Outline each Plasmodium ovale-infected red blood cell.
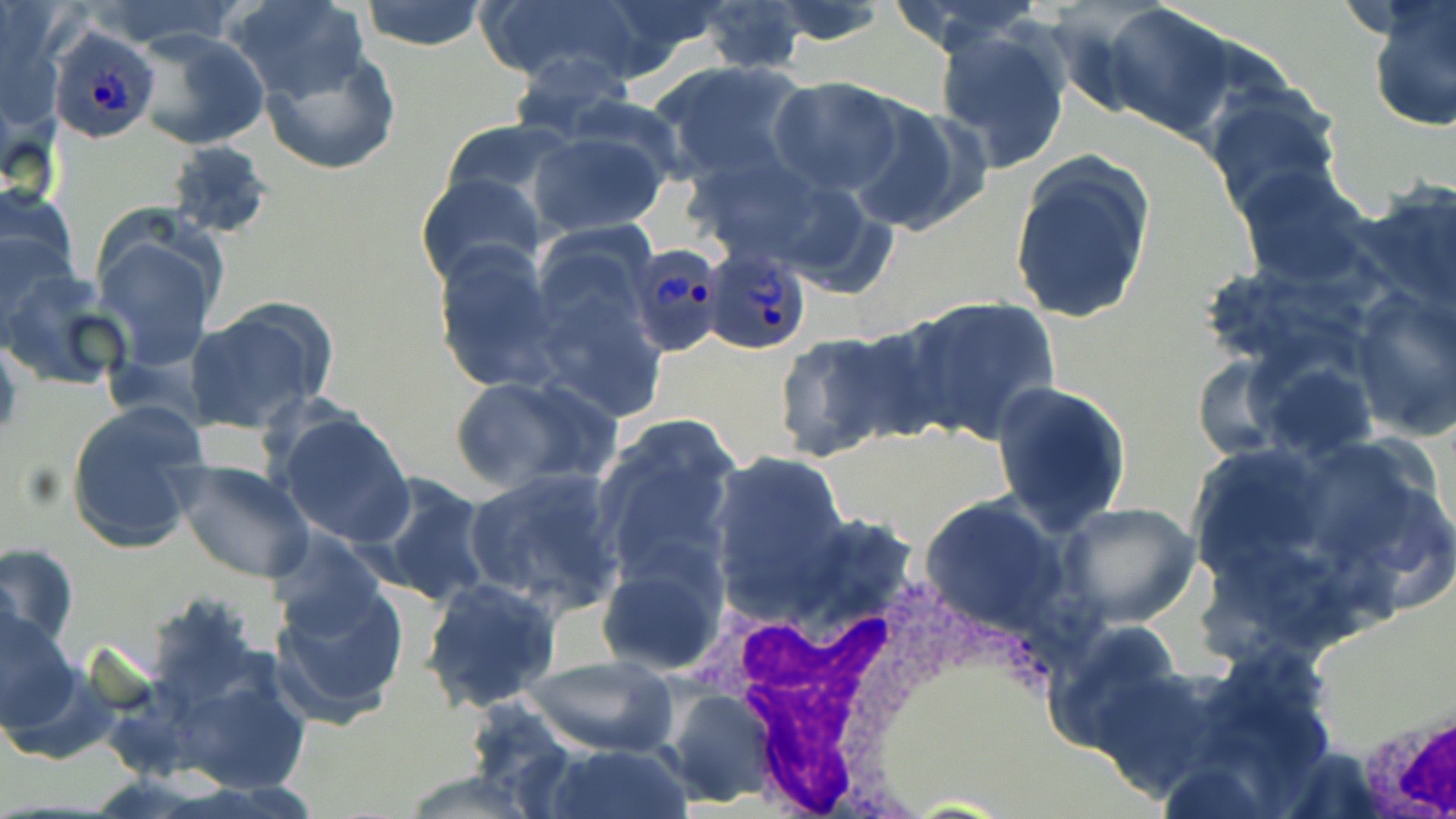

Approximate bounding boxes as (x1, y1, x2, y2) in pixels.
Plasmodium ovale-infected red blood cells: (47, 25, 163, 145), (633, 241, 726, 360), (701, 246, 815, 357).

Summary:
  - White blood cell locations: (716, 559, 998, 815), (1356, 697, 1456, 814)
  - Uninfected red blood cell locations: (227, 0, 373, 105), (357, 0, 489, 52), (475, 0, 652, 91), (883, 0, 1050, 54), (1365, 0, 1455, 132), (693, 1, 811, 75), (764, 2, 894, 47), (1102, 2, 1236, 141), (933, 25, 1072, 174), (131, 29, 269, 152), (261, 51, 400, 177), (505, 52, 638, 140), (651, 58, 814, 188), (768, 76, 909, 198), (1199, 85, 1345, 217), (847, 99, 988, 238), (438, 119, 583, 216), (527, 124, 673, 237), (165, 139, 273, 241), (1009, 154, 1155, 324), (1234, 165, 1373, 290), (416, 173, 548, 292), (1356, 179, 1456, 310), (1, 185, 83, 319), (92, 221, 225, 372), (431, 242, 563, 392), (2, 273, 134, 393), (1347, 288, 1456, 441), (897, 296, 1062, 445), (181, 298, 336, 436), (771, 330, 912, 462), (0, 338, 22, 447), (1188, 350, 1297, 460), (1253, 359, 1382, 463), (447, 373, 614, 493), (991, 379, 1132, 535), (65, 401, 209, 556), (270, 408, 415, 548), (591, 415, 743, 587), (1188, 432, 1456, 635), (1184, 443, 1337, 589), (705, 453, 849, 608), (171, 460, 314, 583), (463, 467, 627, 616), (356, 473, 496, 608), (918, 497, 1077, 640), (1057, 502, 1203, 629), (0, 542, 79, 658), (595, 550, 730, 675), (266, 567, 411, 725), (420, 577, 560, 712), (0, 604, 82, 742), (1044, 620, 1188, 753), (150, 650, 316, 802), (526, 653, 677, 757), (659, 687, 778, 807), (541, 743, 691, 819), (394, 769, 550, 818)
  - Slide-level diagnosis: Plasmodium ovale
  - Stain: May-Grünwald-Giemsa
  - Image size: 1456×819 pixels
  - Field of view: single
  - Preparation: thin blood film
  - Magnification: 1000x
  - Modality: optical microscopy